Report the malaria status of this cell.
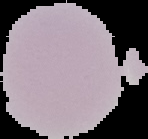
Uninfected.

image_size: 148×139 pixels
image_type: segmented cell region on a black background
preparation: thin blood film